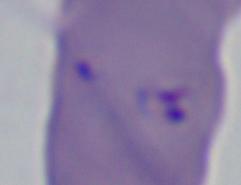
magnification: 1000x
modality: photomicrograph
identification: Babesia